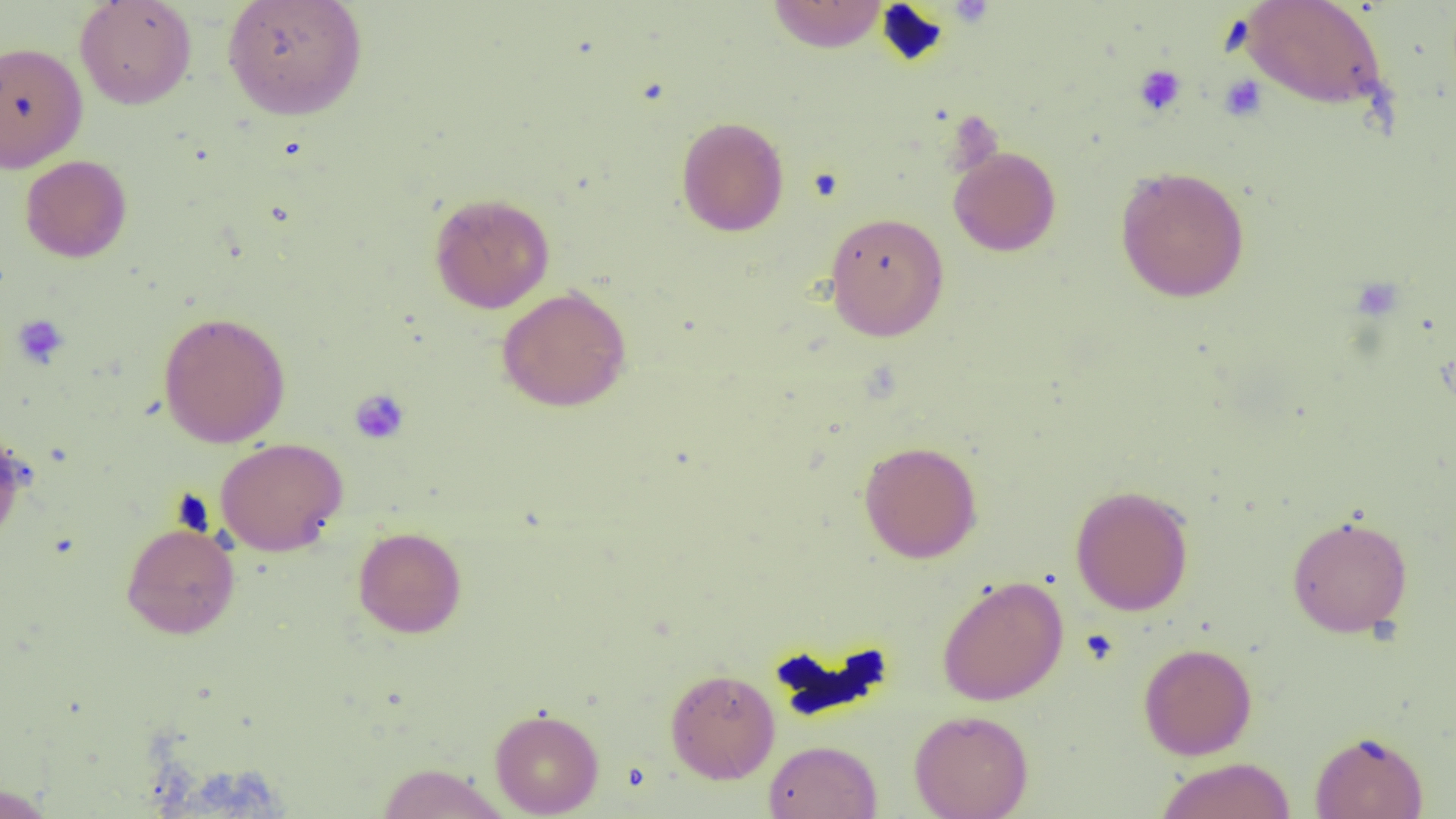 Approximate bounding boxes as [x1, y1, x2, y2] in pixels. Uninfected red blood cell locations: [74, 0, 197, 110], [222, 0, 368, 120], [766, 0, 889, 52], [1240, 0, 1389, 113], [0, 40, 88, 172], [676, 116, 789, 237], [948, 146, 1061, 256], [20, 155, 132, 263], [1114, 165, 1250, 303], [429, 192, 555, 314], [823, 211, 950, 341], [496, 286, 632, 412], [157, 311, 291, 448], [0, 425, 29, 550], [215, 437, 348, 556], [858, 440, 982, 563], [1070, 484, 1195, 616], [1286, 514, 1413, 637], [121, 520, 240, 639], [353, 526, 467, 638], [937, 575, 1068, 706], [1138, 642, 1257, 760], [665, 668, 780, 784], [489, 708, 604, 817], [909, 709, 1034, 819], [1309, 730, 1429, 819], [764, 739, 882, 819], [1154, 757, 1297, 819], [375, 762, 510, 818], [0, 783, 56, 819]. Platelet locations: [945, 1, 996, 29], [1133, 64, 1187, 116], [1218, 75, 1267, 122], [1350, 277, 1403, 321], [12, 314, 70, 369], [349, 389, 410, 445]. Slide-level diagnosis: negative for blood parasites. Captured at 1000x magnification. Thin blood smear. One field of a larger specimen. Image is 1456×819 pixels. Optical microscopy.